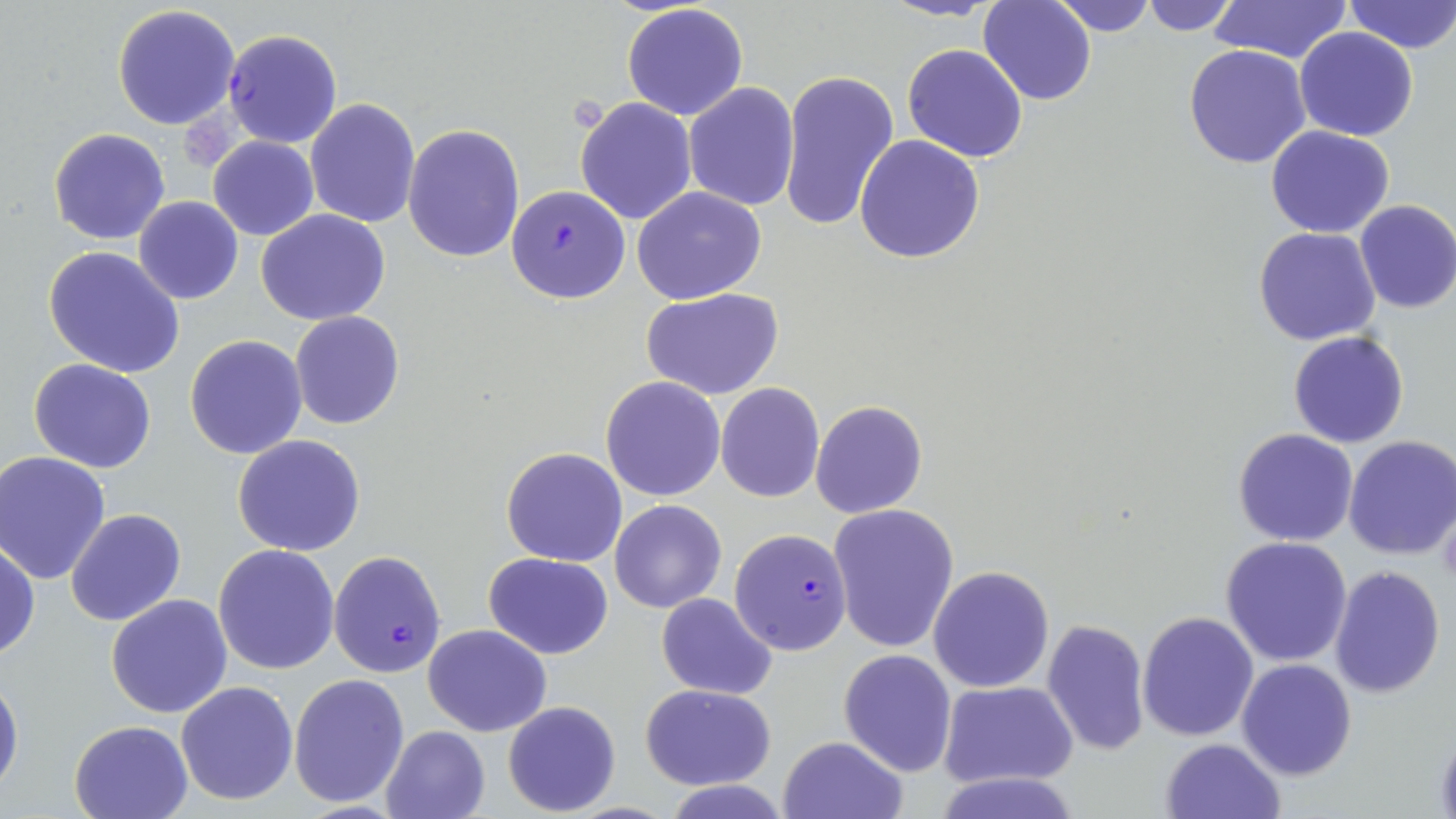
slide-level diagnosis = Plasmodium falciparum
stain = May-Grünwald-Giemsa
uninfected red blood cell locations = approximate bounding boxes as [x1, y1, x2, y2] in pixels: [878, 0, 1007, 22], [1049, 0, 1157, 36], [1138, 0, 1241, 35], [1212, 0, 1352, 65], [1344, 0, 1456, 53], [979, 1, 1097, 105], [622, 3, 749, 119], [112, 5, 242, 130], [1295, 28, 1419, 143], [902, 43, 1029, 163], [1184, 45, 1312, 168], [777, 68, 899, 233], [682, 82, 799, 212], [305, 97, 419, 228], [574, 97, 698, 224], [404, 123, 526, 264], [1266, 125, 1395, 239], [48, 128, 171, 245], [855, 134, 985, 264], [207, 136, 319, 240], [632, 186, 767, 303], [133, 197, 243, 304], [1353, 198, 1456, 314], [256, 209, 391, 326], [1253, 228, 1380, 347], [44, 246, 184, 378], [642, 287, 784, 400], [289, 312, 405, 429], [667, 324, 812, 474], [1287, 330, 1410, 448], [185, 335, 307, 458], [29, 359, 156, 473], [602, 376, 724, 501], [716, 384, 824, 501], [811, 400, 927, 518], [1232, 429, 1359, 547], [232, 435, 365, 556], [1344, 435, 1456, 560], [501, 446, 628, 566], [1, 451, 111, 584], [1437, 498, 1456, 593], [609, 499, 726, 612], [830, 504, 959, 654], [64, 509, 186, 627], [1219, 536, 1353, 668], [1, 540, 39, 661], [213, 545, 340, 675], [483, 552, 614, 659], [927, 565, 1055, 694], [1329, 565, 1446, 699], [105, 593, 233, 718], [656, 593, 777, 699], [1136, 610, 1259, 741], [1041, 617, 1152, 755], [423, 625, 551, 736], [839, 650, 957, 776], [1237, 658, 1357, 781], [0, 671, 23, 802], [289, 673, 410, 807], [175, 680, 300, 805], [940, 680, 1079, 787], [640, 684, 776, 789], [502, 701, 622, 816], [67, 719, 192, 818], [379, 725, 490, 819], [777, 736, 908, 819], [1161, 737, 1285, 819], [932, 769, 1081, 819]
magnification = 1000x
preparation = thin blood film
platelet locations = approximate bounding boxes as [x1, y1, x2, y2] in pixels: [184, 114, 236, 170]
field of view = one of a larger specimen
modality = light microscopy
image size = 1456×819 pixels
Plasmodium falciparum-infected red blood cell locations = approximate bounding boxes as [x1, y1, x2, y2] in pixels: [224, 29, 342, 148], [505, 184, 630, 303], [730, 528, 854, 656], [328, 550, 447, 677]